Locate every Plasmodium parasite.
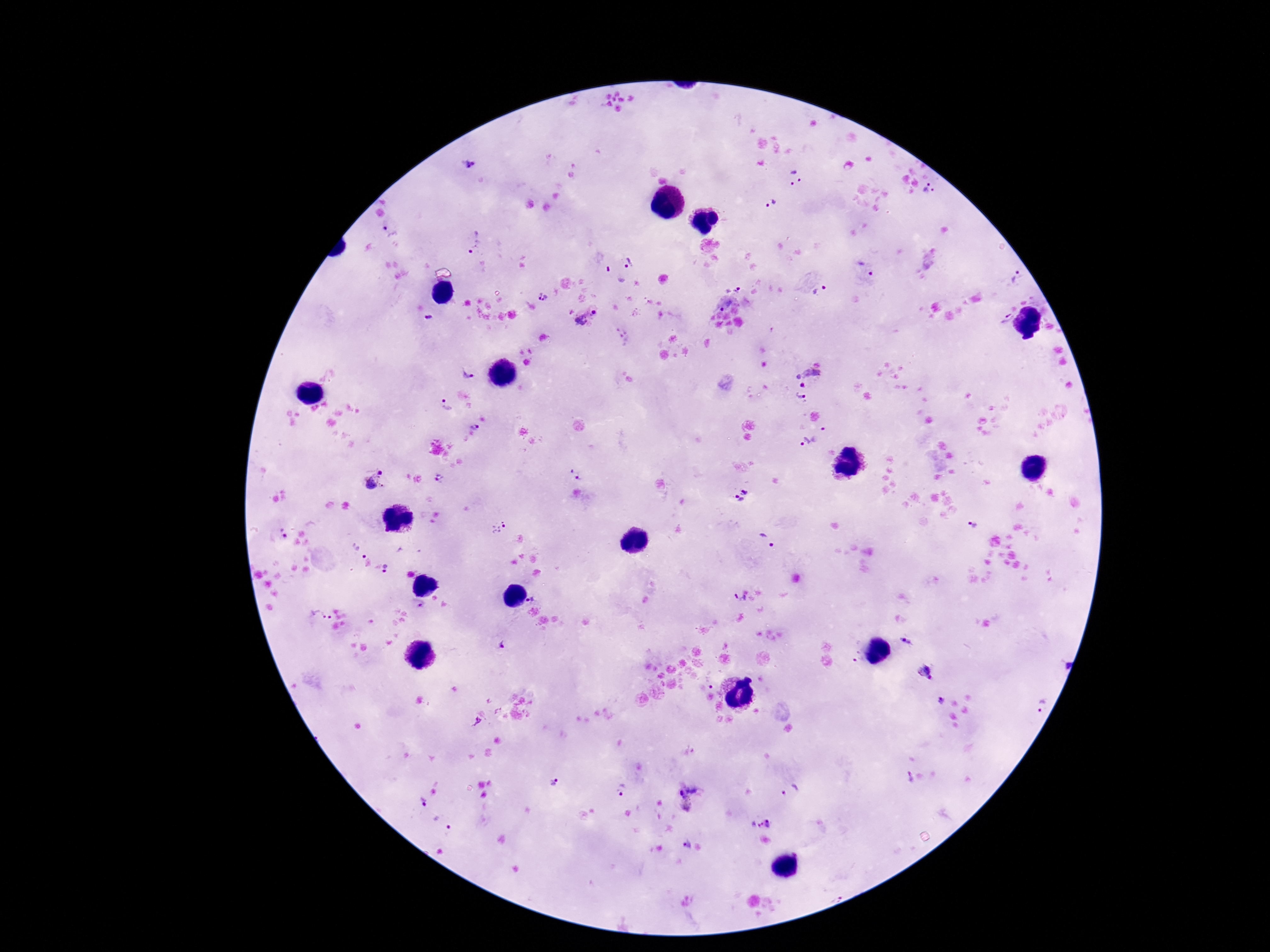
Approximate centers as (x, y) in pixels.
Plasmodium parasites: (470, 164), (795, 179), (928, 188), (771, 203), (393, 236), (471, 240), (629, 263), (865, 269), (1017, 277), (737, 289), (819, 292), (542, 296), (723, 308), (593, 313), (428, 318), (1007, 318), (581, 319), (469, 371), (809, 379), (801, 397), (446, 406), (475, 427), (823, 429), (808, 442), (379, 473), (576, 475), (440, 478), (371, 483), (739, 495), (972, 525), (499, 526), (285, 537), (764, 540), (363, 556), (386, 568), (737, 598), (534, 600), (420, 604), (322, 616), (907, 641), (503, 645), (857, 658), (924, 672), (940, 701), (1041, 706), (909, 777), (554, 780), (621, 790), (790, 790), (680, 791), (425, 804), (687, 805), (760, 821), (449, 831), (685, 844).

Summary:
  - Field of view: one from this slide
  - Preparation: thick blood film
  - Image size: 1270×952 pixels
  - Capture: smartphone camera through the microscope eyepiece
  - Patient malaria status: positive
  - Magnification: 100x
  - Stain: Giemsa